Report the malaria status of this cell.
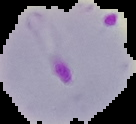
It is parasitized.

image_type: segmented cell region with the area outside set to black
preparation: thin blood smear
image_size: 136×124 pixels